Name the parasite shown.
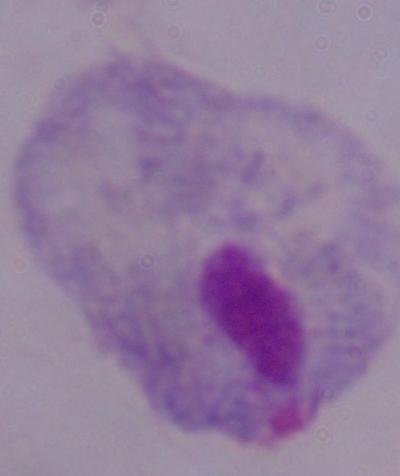

This is a trichomonad.

Micrograph. Captured at 1000x magnification.